Identify the parasite.
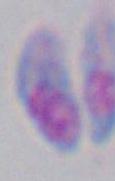

Toxoplasma gondii.

Summary:
  - Magnification: 1000x
  - Modality: micrograph